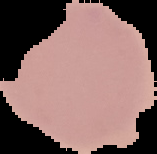

image_type: segmented cell region on a black background
result: no Plasmodium parasites detected
image_size: 157×154 pixels
preparation: thin blood smear